Give the extent of all uninfected red blood cells.
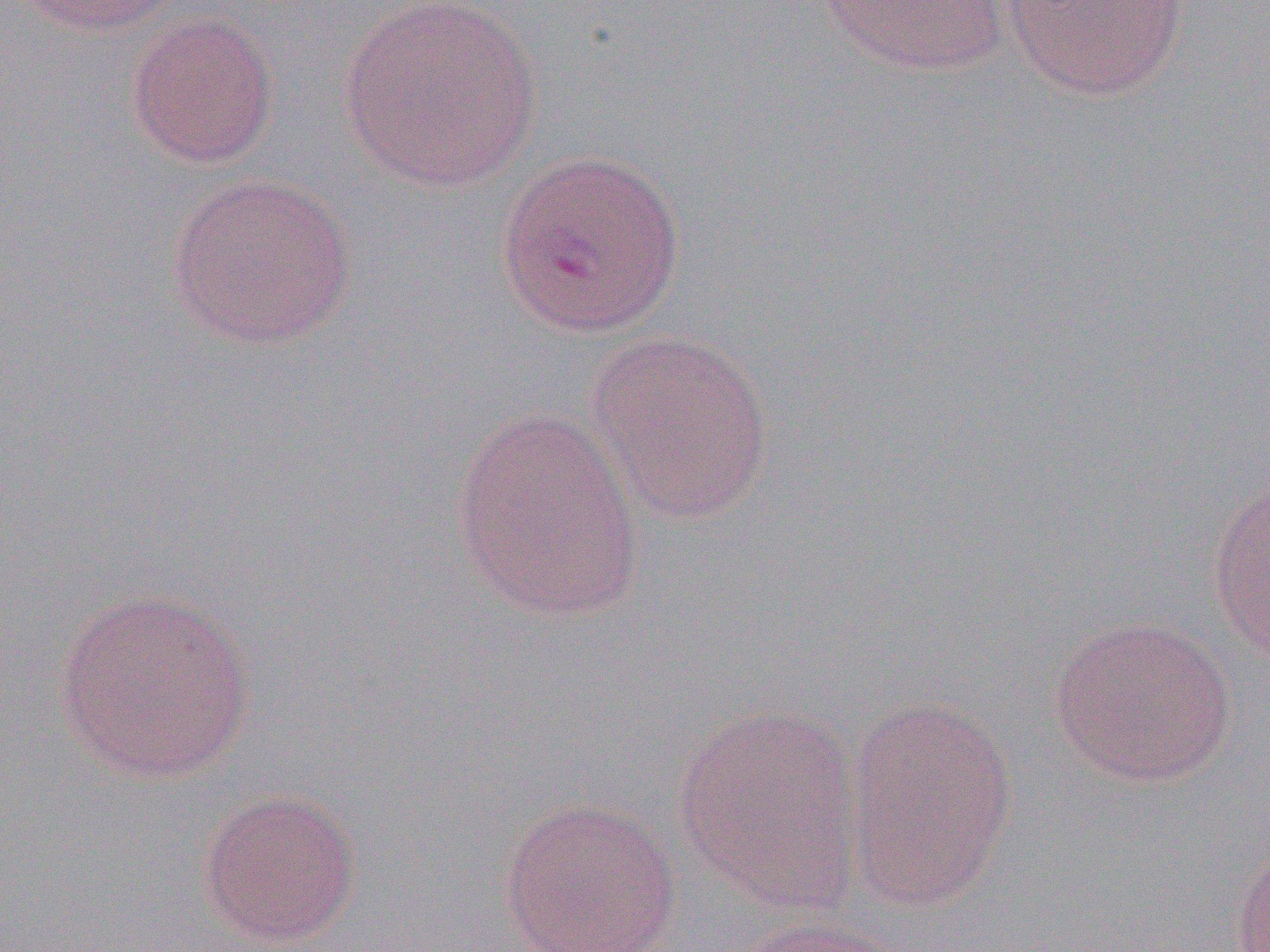

Approximate bounding boxes as named x1/y1/x2/y2 corners in pixels.
Uninfected red blood cells: (x1=13, y1=0, x2=186, y2=37), (x1=339, y1=0, x2=544, y2=193), (x1=818, y1=0, x2=1012, y2=76), (x1=999, y1=0, x2=1190, y2=99), (x1=125, y1=11, x2=280, y2=170), (x1=494, y1=148, x2=687, y2=339), (x1=165, y1=173, x2=356, y2=351), (x1=583, y1=330, x2=775, y2=524), (x1=450, y1=407, x2=646, y2=623), (x1=1206, y1=476, x2=1270, y2=666), (x1=52, y1=588, x2=256, y2=786), (x1=1048, y1=616, x2=1238, y2=788), (x1=841, y1=697, x2=1019, y2=910), (x1=673, y1=703, x2=866, y2=913), (x1=196, y1=788, x2=363, y2=948), (x1=497, y1=797, x2=683, y2=952), (x1=1229, y1=843, x2=1270, y2=952), (x1=729, y1=916, x2=908, y2=952).

Slide-level diagnosis: Plasmodium vivax. Image is 1270×952 pixels. Thin blood film. Single field of view. Optical microscopy. Captured at 1000x magnification.